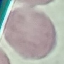

Summary:
  - Result: negative for malaria parasites
  - Image type: automatically extracted cell patch, resized to 64 × 64 pixels
  - Stain: Giemsa
  - Capture: smartphone camera at the microscope eyepiece
  - Preparation: thin blood film